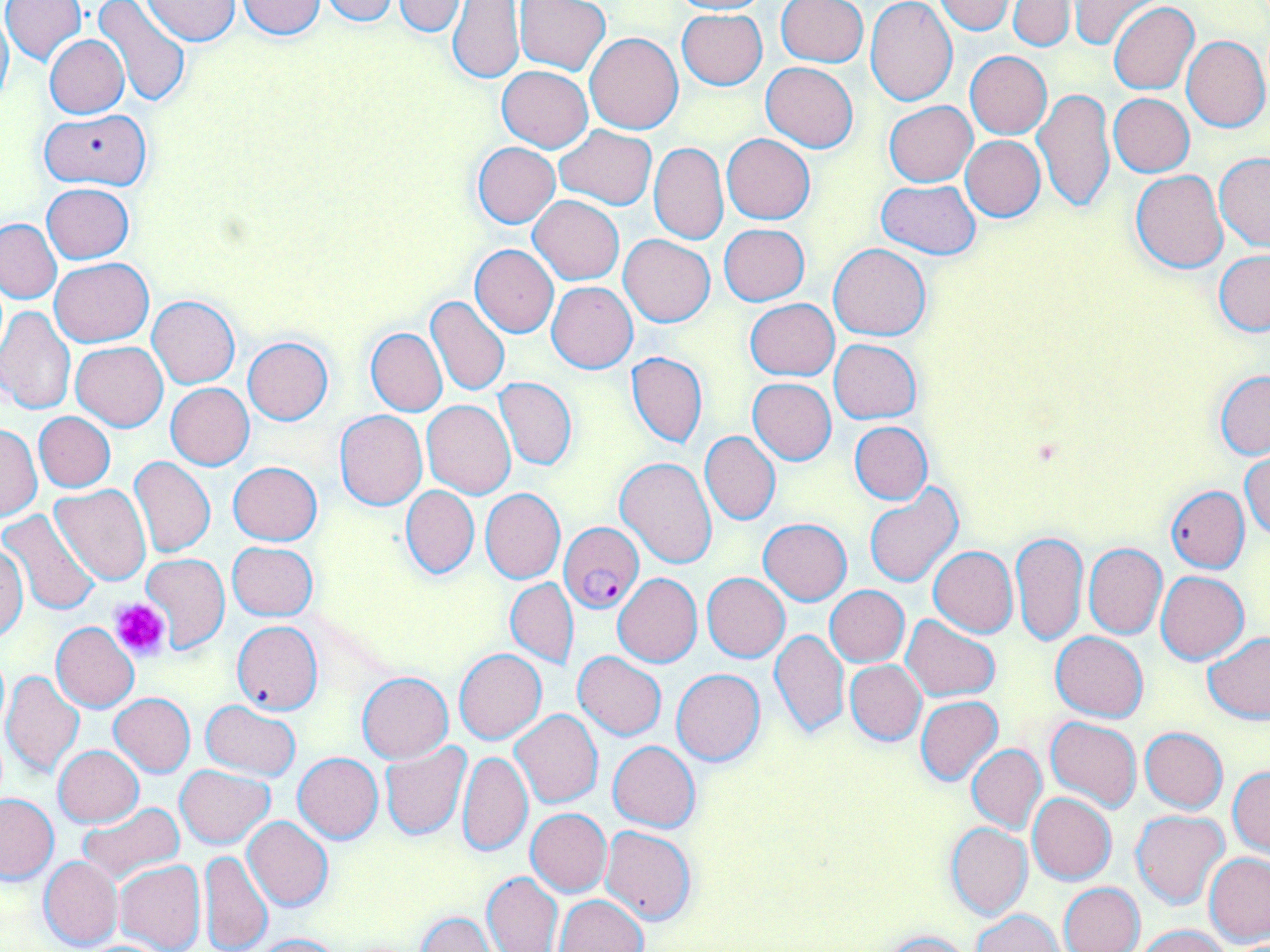
Summary:
  - Coordinate format: approximate bounding boxes as [x1, y1, x2, y2] in pixels
  - Uninfected red blood cell locations (subset): [2, 0, 86, 65], [92, 0, 190, 105], [320, 0, 398, 24], [515, 0, 609, 75], [668, 0, 773, 15], [865, 0, 957, 105], [1070, 0, 1156, 51], [141, 1, 239, 45], [236, 1, 328, 39], [391, 1, 468, 37], [447, 1, 526, 83], [776, 1, 867, 68], [932, 1, 1015, 34], [1008, 1, 1074, 52], [1108, 3, 1199, 93], [0, 9, 13, 110], [676, 9, 767, 90], [585, 32, 683, 133], [1182, 34, 1269, 132], [44, 35, 128, 118], [964, 51, 1052, 138], [761, 63, 858, 152], [497, 65, 592, 152], [1032, 87, 1115, 214], [1108, 93, 1194, 176], [884, 101, 977, 186], [41, 108, 149, 190], [554, 125, 658, 209], [722, 134, 814, 223], [961, 135, 1046, 221], [472, 143, 560, 228], [649, 143, 729, 245], [1215, 153, 1270, 252], [1131, 170, 1229, 273], [875, 179, 982, 258], [42, 183, 134, 262], [529, 196, 624, 284], [0, 218, 62, 303], [719, 223, 809, 306], [618, 234, 715, 327], [829, 243, 931, 341], [470, 244, 559, 337], [1214, 249, 1270, 335], [51, 258, 153, 346], [547, 282, 637, 373], [148, 295, 240, 388], [426, 296, 509, 396], [744, 299, 840, 380], [0, 306, 75, 417], [366, 328, 446, 416], [243, 336, 334, 424], [829, 339, 921, 423], [71, 341, 168, 430], [626, 351, 707, 449], [1214, 372, 1269, 459], [494, 377, 577, 470], [747, 378, 836, 465], [166, 383, 254, 470], [422, 400, 515, 498], [335, 411, 427, 510], [34, 412, 115, 491], [850, 422, 932, 504], [1, 423, 41, 522], [701, 432, 780, 526], [1242, 451, 1270, 540], [130, 456, 215, 557], [614, 456, 716, 568], [228, 462, 321, 545], [50, 484, 151, 586], [401, 485, 478, 579], [864, 486, 962, 587], [1166, 486, 1250, 573], [480, 488, 565, 583], [0, 508, 101, 614], [760, 518, 851, 604], [1011, 530, 1087, 646], [227, 541, 318, 620], [1083, 543, 1166, 639], [928, 546, 1017, 638], [1, 547, 27, 638], [141, 554, 231, 654], [1156, 571, 1249, 664], [702, 572, 790, 662], [613, 573, 702, 667], [505, 578, 578, 669], [826, 586, 909, 666], [900, 614, 1000, 701], [232, 621, 322, 714], [52, 623, 139, 712], [769, 629, 849, 738], [1202, 630, 1270, 723], [1051, 632, 1148, 721], [454, 647, 547, 744], [573, 652, 667, 740], [845, 659, 926, 746], [672, 669, 765, 767], [3, 670, 85, 779], [358, 672, 453, 762], [109, 693, 196, 776], [915, 696, 1002, 786], [200, 700, 301, 781], [511, 710, 603, 809], [1046, 717, 1142, 811], [1140, 727, 1227, 812], [608, 740, 701, 831], [380, 743, 471, 840], [967, 744, 1046, 833], [54, 745, 143, 827], [459, 750, 533, 859], [293, 752, 383, 843], [176, 765, 273, 847], [1228, 765, 1270, 857], [1027, 792, 1116, 885], [0, 793, 58, 882], [78, 802, 184, 886], [526, 809, 611, 896], [1132, 812, 1231, 909], [244, 816, 333, 911], [946, 823, 1032, 919], [601, 825, 697, 924], [199, 851, 272, 952], [1204, 852, 1270, 945], [39, 857, 123, 950], [115, 860, 206, 952], [481, 871, 563, 952], [1058, 882, 1144, 952], [554, 896, 648, 952], [973, 910, 1063, 952], [414, 912, 496, 952], [1135, 924, 1233, 952], [877, 929, 973, 951], [246, 933, 344, 952]
  - Platelet locations: [111, 598, 170, 662]
  - Slide-level diagnosis: Plasmodium falciparum
  - Modality: light microscopy
  - Preparation: thin blood film
  - Magnification: 1000x
  - Field of view: one of a larger specimen
  - Stain: May-Grünwald-Giemsa
  - Image size: 1270×952 pixels